Locate every blood parasite and identify its species.
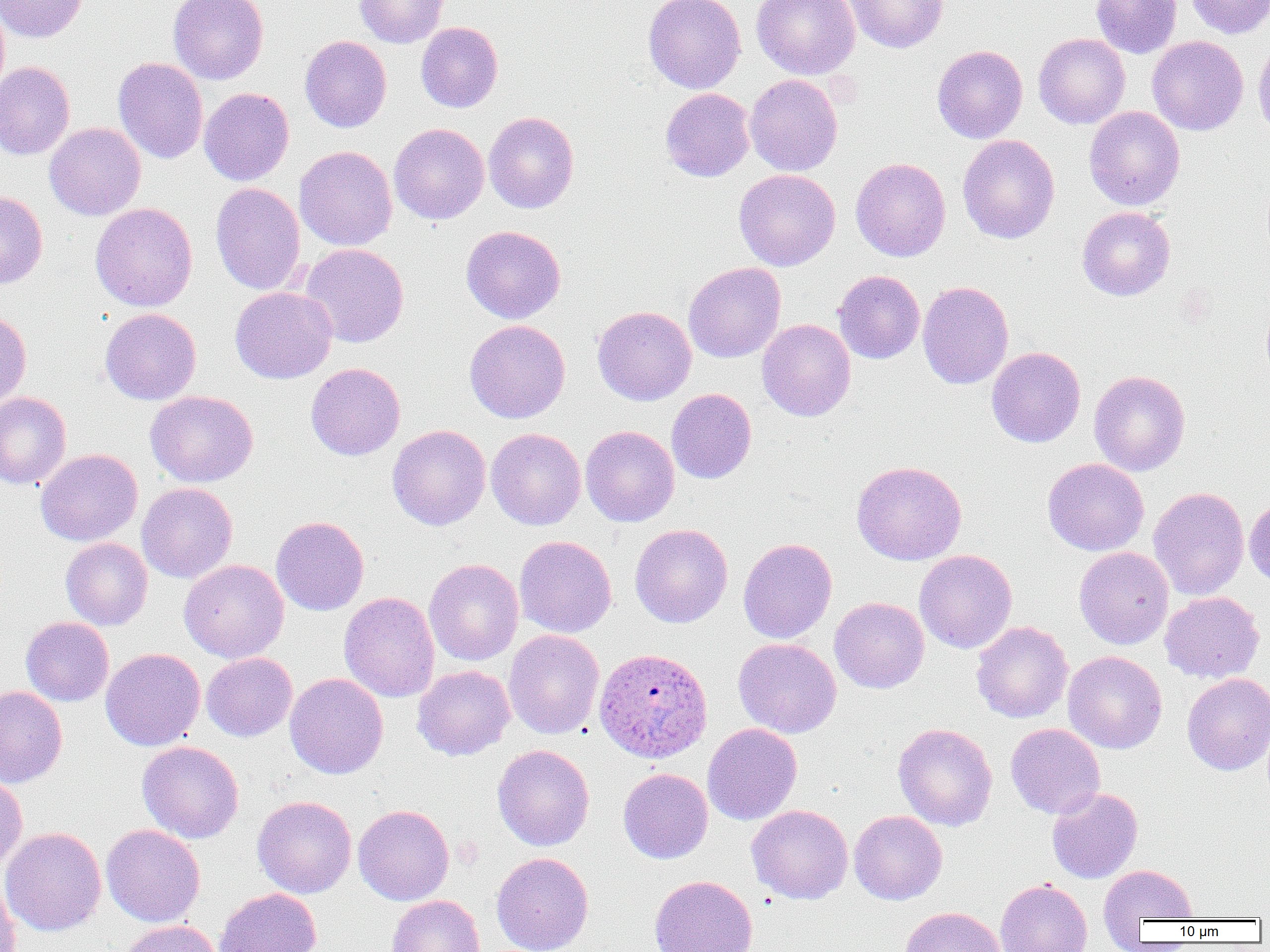
Approximate bounding boxes as (x1, y1, x2, y2) in pixels.
Plasmodium ovale-infected red blood cells: (594, 647, 712, 763).
No Plasmodium falciparum, Plasmodium malariae, Plasmodium vivax, Babesia divergens, or Trypanosoma brucei observed.

Uninfected red blood cell locations: (0, 0, 88, 43), (168, 0, 269, 84), (354, 0, 448, 48), (643, 0, 746, 93), (752, 0, 860, 79), (846, 0, 948, 53), (1091, 0, 1181, 58), (1185, 0, 1270, 39), (416, 22, 503, 112), (1033, 33, 1130, 129), (300, 35, 392, 132), (1147, 36, 1248, 136), (1253, 36, 1270, 138), (932, 45, 1028, 143), (113, 57, 208, 164), (0, 61, 74, 160), (744, 74, 843, 176), (199, 87, 294, 186), (660, 88, 755, 182), (1084, 106, 1185, 211), (483, 111, 580, 214), (44, 122, 146, 220), (389, 123, 489, 224), (957, 134, 1060, 244), (294, 146, 397, 251), (850, 157, 951, 262), (733, 169, 841, 271), (210, 182, 306, 295), (0, 190, 48, 289), (90, 202, 198, 311), (1077, 206, 1175, 300), (460, 225, 566, 323), (300, 243, 409, 347), (683, 262, 786, 363), (833, 270, 925, 364), (917, 280, 1014, 390), (230, 286, 337, 384), (592, 305, 697, 406), (100, 308, 201, 405), (0, 309, 31, 411), (464, 319, 570, 424), (757, 319, 856, 421), (986, 347, 1086, 447), (305, 363, 405, 461), (1089, 370, 1190, 476), (666, 388, 757, 484), (145, 390, 258, 487), (0, 392, 72, 490), (387, 425, 491, 531), (580, 425, 679, 527), (486, 428, 586, 530), (36, 448, 143, 546), (1042, 458, 1149, 556), (851, 460, 967, 565), (137, 482, 238, 583), (1148, 486, 1249, 600), (1244, 497, 1270, 589), (271, 515, 369, 616), (629, 524, 733, 628), (514, 535, 617, 638), (60, 537, 153, 630), (738, 538, 837, 644), (1074, 546, 1174, 649), (914, 549, 1017, 654), (179, 559, 289, 663), (424, 559, 524, 665), (339, 591, 439, 702), (1159, 591, 1265, 683), (830, 596, 930, 694), (21, 616, 114, 706), (971, 621, 1073, 723), (503, 629, 604, 739), (733, 638, 842, 738), (100, 647, 205, 751), (1063, 651, 1167, 754), (201, 652, 297, 742), (412, 665, 515, 760), (285, 672, 388, 779), (1182, 673, 1270, 775), (0, 686, 68, 788), (893, 722, 997, 831), (703, 723, 802, 826), (1005, 723, 1105, 818), (137, 741, 244, 843), (492, 744, 595, 851), (618, 768, 713, 864), (0, 771, 28, 872), (1046, 787, 1143, 883), (252, 795, 356, 898), (353, 805, 454, 906), (746, 805, 853, 904), (849, 810, 947, 905), (101, 824, 205, 927), (1, 827, 107, 936), (491, 852, 594, 952), (1099, 864, 1199, 928), (0, 873, 20, 952), (649, 875, 758, 952), (995, 879, 1092, 952), (214, 887, 322, 952), (387, 895, 485, 952), (898, 906, 1006, 952), (117, 920, 221, 952). Slide-level diagnosis: Plasmodium ovale. Image is 1270×952 pixels. Thin blood smear. Single field of view. 1000x magnification. Optical microscopy.